State which parasite is depicted.
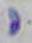
This is Toxoplasma gondii.

magnification = 1000x
modality = photomicrograph